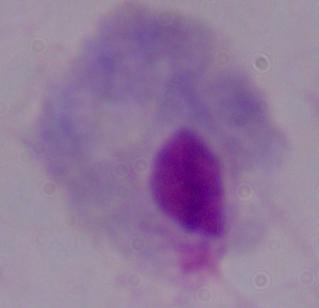

magnification: 1000x
modality: photomicrograph
identification: trichomonad